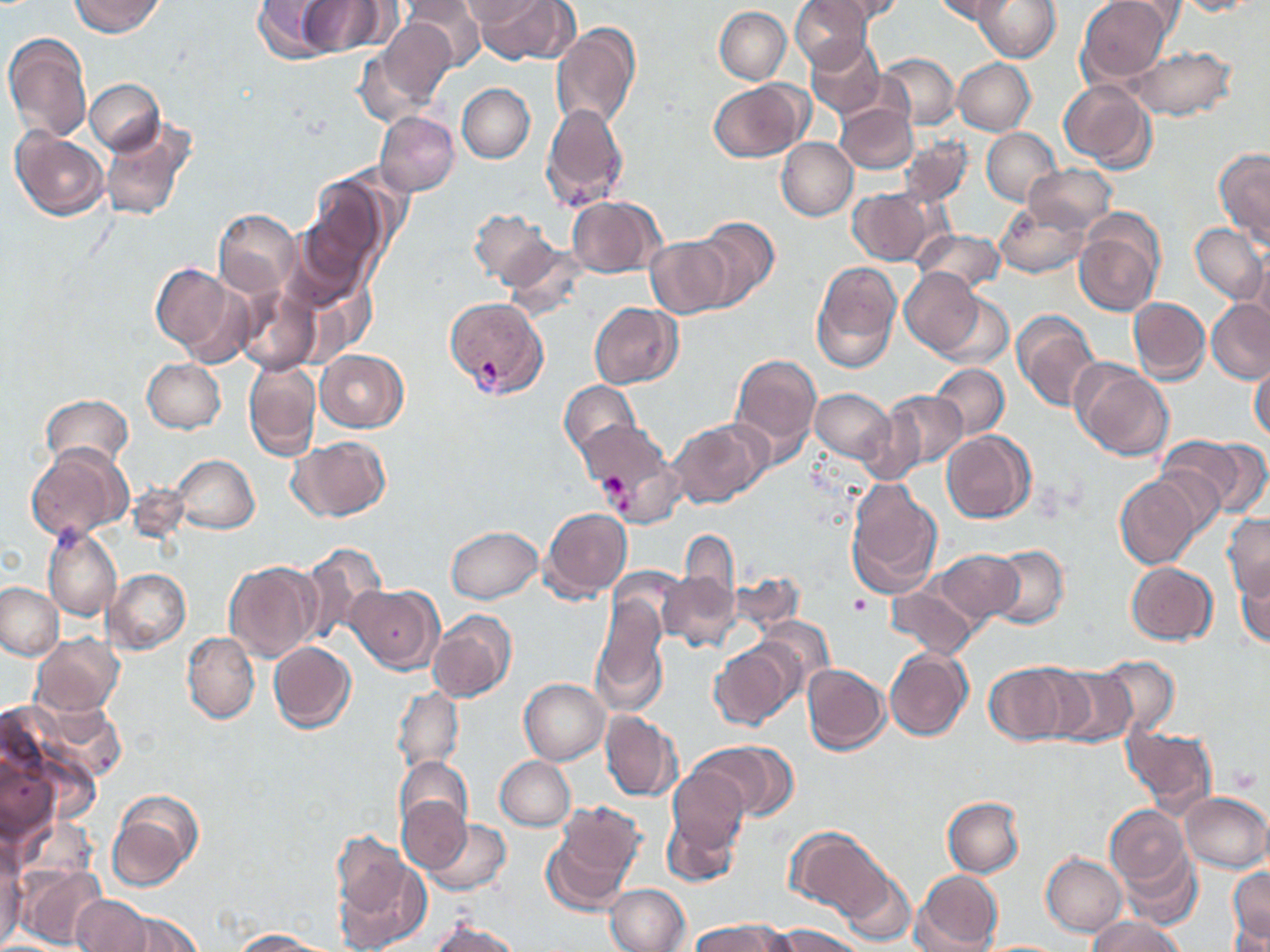

Summary:
  - Coordinate format: approximate bounding boxes as named x1/y1/x2/y2 corners in pixels
  - Platelet locations: (x1=598, y1=473, x2=626, y2=498), (x1=850, y1=594, x2=872, y2=617), (x1=1230, y1=769, x2=1259, y2=793)
  - Plasmodium vivax-infected red blood cell locations: (x1=444, y1=297, x2=546, y2=398)
  - Uninfected red blood cell locations: (x1=70, y1=0, x2=163, y2=36), (x1=252, y1=0, x2=336, y2=62), (x1=406, y1=0, x2=486, y2=72), (x1=461, y1=0, x2=546, y2=27), (x1=473, y1=0, x2=575, y2=63), (x1=792, y1=0, x2=873, y2=70), (x1=805, y1=0, x2=904, y2=28), (x1=930, y1=0, x2=1019, y2=26), (x1=973, y1=0, x2=1061, y2=63), (x1=1071, y1=0, x2=1169, y2=165), (x1=1079, y1=0, x2=1174, y2=81), (x1=1173, y1=1, x2=1262, y2=17), (x1=298, y1=2, x2=384, y2=53), (x1=715, y1=6, x2=791, y2=84), (x1=376, y1=18, x2=459, y2=108), (x1=552, y1=21, x2=642, y2=132), (x1=3, y1=32, x2=91, y2=146), (x1=807, y1=35, x2=885, y2=120), (x1=355, y1=40, x2=446, y2=132), (x1=1130, y1=45, x2=1235, y2=120), (x1=878, y1=54, x2=961, y2=129), (x1=953, y1=57, x2=1034, y2=134), (x1=707, y1=78, x2=811, y2=162), (x1=87, y1=79, x2=165, y2=154), (x1=1059, y1=80, x2=1156, y2=170), (x1=457, y1=83, x2=535, y2=163), (x1=541, y1=103, x2=629, y2=209), (x1=838, y1=103, x2=917, y2=174), (x1=375, y1=111, x2=459, y2=196), (x1=98, y1=115, x2=197, y2=223), (x1=11, y1=126, x2=110, y2=222), (x1=981, y1=126, x2=1061, y2=206), (x1=897, y1=133, x2=971, y2=208), (x1=777, y1=138, x2=858, y2=220), (x1=1215, y1=147, x2=1269, y2=250), (x1=1029, y1=163, x2=1116, y2=233), (x1=299, y1=180, x2=387, y2=296), (x1=849, y1=188, x2=937, y2=265), (x1=566, y1=195, x2=664, y2=278), (x1=994, y1=199, x2=1090, y2=279), (x1=469, y1=208, x2=559, y2=291), (x1=214, y1=210, x2=301, y2=299), (x1=692, y1=216, x2=779, y2=309), (x1=1074, y1=217, x2=1163, y2=317), (x1=1190, y1=222, x2=1266, y2=305), (x1=915, y1=227, x2=1005, y2=293), (x1=647, y1=234, x2=733, y2=318), (x1=1250, y1=252, x2=1270, y2=333), (x1=810, y1=261, x2=903, y2=374), (x1=150, y1=263, x2=235, y2=356), (x1=900, y1=269, x2=987, y2=356), (x1=235, y1=285, x2=321, y2=375), (x1=938, y1=291, x2=1011, y2=368), (x1=1128, y1=297, x2=1210, y2=384), (x1=1205, y1=298, x2=1269, y2=383), (x1=588, y1=301, x2=682, y2=388), (x1=1012, y1=308, x2=1102, y2=413), (x1=316, y1=349, x2=407, y2=432), (x1=729, y1=352, x2=823, y2=462), (x1=141, y1=356, x2=225, y2=432), (x1=243, y1=359, x2=321, y2=460), (x1=1074, y1=363, x2=1173, y2=461), (x1=929, y1=364, x2=1008, y2=441), (x1=1249, y1=364, x2=1269, y2=443), (x1=561, y1=380, x2=642, y2=462), (x1=810, y1=387, x2=896, y2=466), (x1=879, y1=388, x2=966, y2=474), (x1=42, y1=394, x2=133, y2=471), (x1=669, y1=418, x2=769, y2=509), (x1=578, y1=419, x2=677, y2=521), (x1=942, y1=431, x2=1035, y2=524), (x1=288, y1=436, x2=391, y2=522), (x1=1159, y1=437, x2=1244, y2=517), (x1=1195, y1=437, x2=1270, y2=518), (x1=26, y1=444, x2=131, y2=542), (x1=174, y1=454, x2=260, y2=534), (x1=1114, y1=473, x2=1204, y2=568), (x1=844, y1=478, x2=945, y2=597), (x1=542, y1=506, x2=633, y2=600), (x1=1223, y1=513, x2=1270, y2=599), (x1=43, y1=525, x2=120, y2=621), (x1=447, y1=525, x2=545, y2=604), (x1=678, y1=530, x2=741, y2=618), (x1=299, y1=540, x2=389, y2=645), (x1=989, y1=544, x2=1069, y2=628), (x1=930, y1=547, x2=1021, y2=628), (x1=224, y1=560, x2=323, y2=662), (x1=1126, y1=560, x2=1218, y2=643), (x1=1234, y1=562, x2=1270, y2=649), (x1=105, y1=567, x2=191, y2=654), (x1=733, y1=571, x2=806, y2=634), (x1=658, y1=573, x2=743, y2=651), (x1=0, y1=581, x2=65, y2=663), (x1=347, y1=584, x2=442, y2=673), (x1=889, y1=585, x2=976, y2=658), (x1=591, y1=600, x2=671, y2=706), (x1=428, y1=608, x2=517, y2=703), (x1=181, y1=630, x2=259, y2=723), (x1=31, y1=632, x2=124, y2=716), (x1=710, y1=639, x2=800, y2=729), (x1=268, y1=641, x2=357, y2=733), (x1=884, y1=647, x2=973, y2=740), (x1=1097, y1=655, x2=1181, y2=738), (x1=803, y1=662, x2=891, y2=755), (x1=985, y1=662, x2=1076, y2=748), (x1=1046, y1=665, x2=1139, y2=748), (x1=520, y1=678, x2=609, y2=763), (x1=392, y1=686, x2=464, y2=778), (x1=30, y1=694, x2=126, y2=783), (x1=599, y1=710, x2=683, y2=801), (x1=1123, y1=723, x2=1219, y2=818), (x1=700, y1=741, x2=794, y2=820), (x1=1, y1=750, x2=57, y2=853), (x1=495, y1=755, x2=575, y2=830), (x1=395, y1=756, x2=473, y2=837), (x1=667, y1=766, x2=751, y2=853), (x1=107, y1=788, x2=205, y2=891), (x1=1180, y1=791, x2=1269, y2=872), (x1=944, y1=795, x2=1024, y2=877), (x1=398, y1=797, x2=469, y2=870), (x1=549, y1=800, x2=646, y2=904), (x1=1104, y1=803, x2=1191, y2=899), (x1=661, y1=808, x2=743, y2=886), (x1=421, y1=815, x2=512, y2=897), (x1=788, y1=826, x2=892, y2=921), (x1=331, y1=849, x2=430, y2=952), (x1=0, y1=850, x2=26, y2=943), (x1=1122, y1=851, x2=1202, y2=930), (x1=1041, y1=852, x2=1128, y2=936), (x1=18, y1=866, x2=108, y2=947), (x1=1228, y1=867, x2=1270, y2=944), (x1=913, y1=869, x2=1003, y2=951), (x1=845, y1=874, x2=913, y2=946), (x1=605, y1=883, x2=688, y2=951), (x1=72, y1=894, x2=152, y2=952), (x1=122, y1=910, x2=204, y2=951), (x1=1086, y1=917, x2=1185, y2=952), (x1=427, y1=921, x2=522, y2=952), (x1=689, y1=921, x2=782, y2=952), (x1=1231, y1=922, x2=1270, y2=951), (x1=769, y1=923, x2=866, y2=952), (x1=229, y1=929, x2=334, y2=950)
  - Slide-level diagnosis: Plasmodium vivax
  - Magnification: 1000x
  - Field of view: one of a larger specimen
  - Modality: optical microscopy
  - Preparation: thin blood smear
  - Stain: May-Grünwald-Giemsa
  - Image size: 1270×952 pixels